Classify this cell by malaria status.
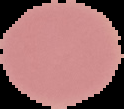

Uninfected.

Summary:
  - Image size: 124×109 pixels
  - Preparation: thin blood film
  - Image type: segmented cell region with the area outside set to black